Locate every blood parasite and identify its species.
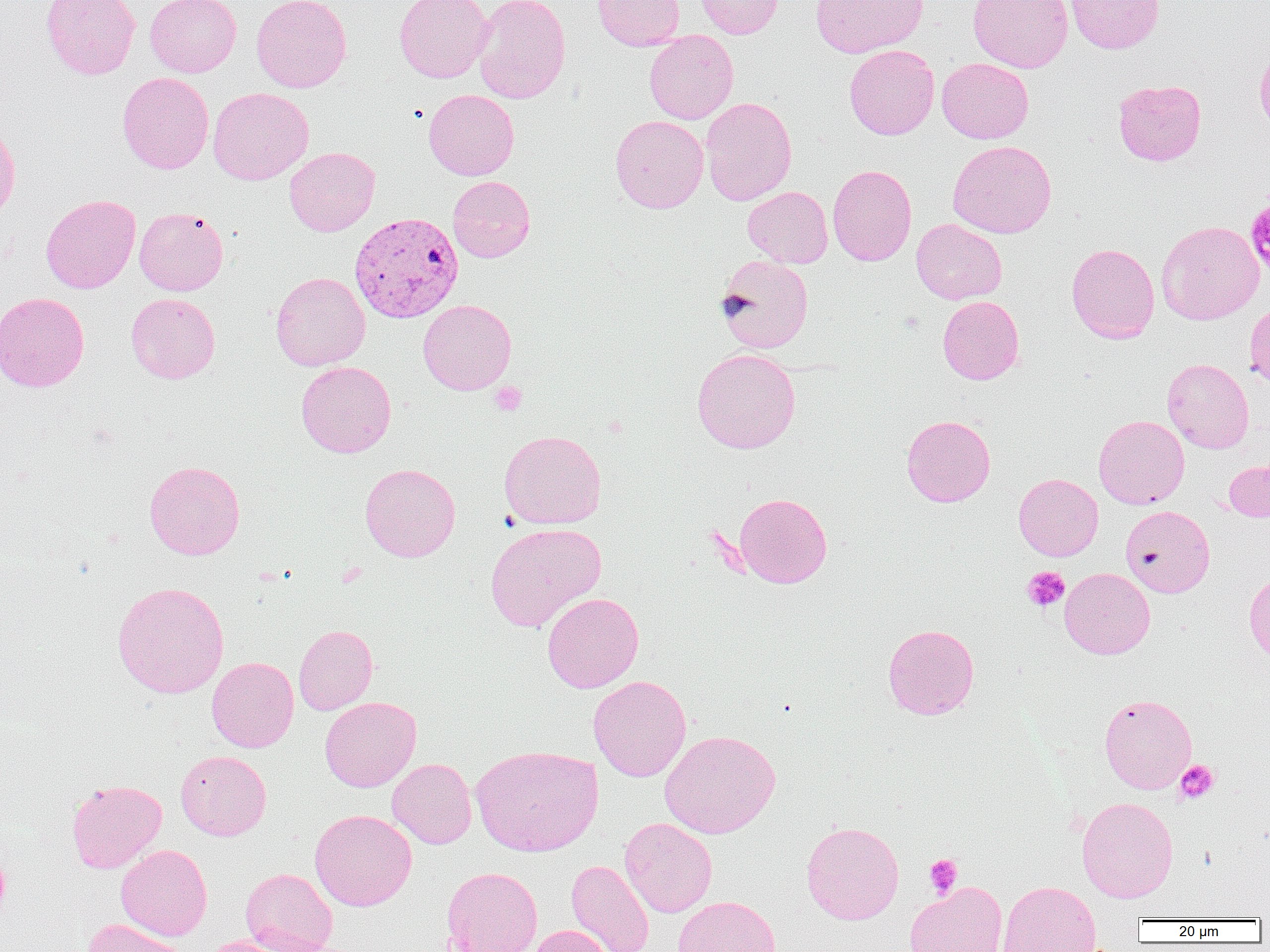

Approximate bounding boxes as named x1/y1/x2/y2 corners in pixels.
Plasmodium vivax-infected red blood cells: (x1=349, y1=211, x2=463, y2=323).
No Plasmodium falciparum, Plasmodium ovale, Plasmodium malariae, Babesia divergens, or Trypanosoma brucei observed.

Platelet locations: (x1=489, y1=381, x2=527, y2=416), (x1=1022, y1=566, x2=1070, y2=612), (x1=1175, y1=760, x2=1219, y2=804), (x1=924, y1=854, x2=962, y2=897). Uninfected red blood cell locations: (x1=40, y1=0, x2=140, y2=80), (x1=145, y1=0, x2=241, y2=77), (x1=251, y1=0, x2=351, y2=93), (x1=394, y1=0, x2=494, y2=83), (x1=472, y1=0, x2=570, y2=104), (x1=592, y1=0, x2=685, y2=50), (x1=696, y1=0, x2=783, y2=39), (x1=811, y1=0, x2=929, y2=58), (x1=967, y1=0, x2=1073, y2=72), (x1=1065, y1=0, x2=1165, y2=54), (x1=644, y1=30, x2=739, y2=124), (x1=1254, y1=44, x2=1270, y2=138), (x1=844, y1=45, x2=939, y2=140), (x1=937, y1=57, x2=1034, y2=144), (x1=117, y1=72, x2=214, y2=174), (x1=1113, y1=79, x2=1206, y2=166), (x1=208, y1=87, x2=314, y2=185), (x1=424, y1=90, x2=519, y2=180), (x1=700, y1=96, x2=797, y2=206), (x1=610, y1=115, x2=709, y2=213), (x1=0, y1=123, x2=20, y2=226), (x1=947, y1=140, x2=1057, y2=238), (x1=284, y1=147, x2=380, y2=236), (x1=828, y1=164, x2=916, y2=265), (x1=448, y1=176, x2=536, y2=262), (x1=743, y1=186, x2=833, y2=268), (x1=41, y1=194, x2=141, y2=293), (x1=134, y1=207, x2=228, y2=296), (x1=911, y1=219, x2=1007, y2=304), (x1=1156, y1=220, x2=1264, y2=325), (x1=1066, y1=242, x2=1159, y2=343), (x1=716, y1=255, x2=814, y2=353), (x1=270, y1=272, x2=370, y2=371), (x1=0, y1=292, x2=89, y2=392), (x1=126, y1=292, x2=220, y2=383), (x1=937, y1=295, x2=1024, y2=385), (x1=418, y1=299, x2=516, y2=395), (x1=1244, y1=302, x2=1270, y2=387), (x1=692, y1=348, x2=801, y2=454), (x1=1162, y1=358, x2=1254, y2=453), (x1=296, y1=361, x2=396, y2=457), (x1=901, y1=415, x2=995, y2=507), (x1=1093, y1=415, x2=1189, y2=509), (x1=499, y1=429, x2=606, y2=529), (x1=1223, y1=459, x2=1270, y2=521), (x1=144, y1=460, x2=245, y2=560), (x1=360, y1=463, x2=460, y2=562), (x1=1014, y1=473, x2=1103, y2=561), (x1=734, y1=492, x2=832, y2=588), (x1=1121, y1=505, x2=1215, y2=597), (x1=485, y1=522, x2=606, y2=631), (x1=1060, y1=567, x2=1155, y2=659), (x1=1244, y1=572, x2=1270, y2=662), (x1=111, y1=581, x2=229, y2=699), (x1=542, y1=592, x2=644, y2=693), (x1=882, y1=623, x2=979, y2=719), (x1=294, y1=624, x2=378, y2=715), (x1=207, y1=657, x2=298, y2=752), (x1=589, y1=675, x2=691, y2=782), (x1=1099, y1=694, x2=1197, y2=794), (x1=320, y1=697, x2=421, y2=792), (x1=660, y1=730, x2=781, y2=838), (x1=470, y1=744, x2=603, y2=856), (x1=175, y1=750, x2=272, y2=840), (x1=387, y1=758, x2=477, y2=849), (x1=66, y1=779, x2=167, y2=873), (x1=1076, y1=796, x2=1178, y2=903), (x1=309, y1=809, x2=416, y2=911), (x1=619, y1=817, x2=717, y2=918), (x1=801, y1=821, x2=904, y2=924), (x1=116, y1=844, x2=212, y2=940), (x1=0, y1=848, x2=10, y2=926), (x1=566, y1=859, x2=654, y2=952), (x1=441, y1=866, x2=543, y2=952), (x1=240, y1=867, x2=338, y2=952), (x1=998, y1=880, x2=1101, y2=952), (x1=904, y1=881, x2=1008, y2=952), (x1=673, y1=895, x2=781, y2=952), (x1=83, y1=918, x2=187, y2=952), (x1=528, y1=925, x2=613, y2=952), (x1=200, y1=935, x2=296, y2=952). Slide-level diagnosis: Plasmodium vivax. 1000x magnification. One field of a larger specimen. Image is 1270×952 pixels. Optical microscopy. Thin blood film.